Locate every blood parasite and identify its species.
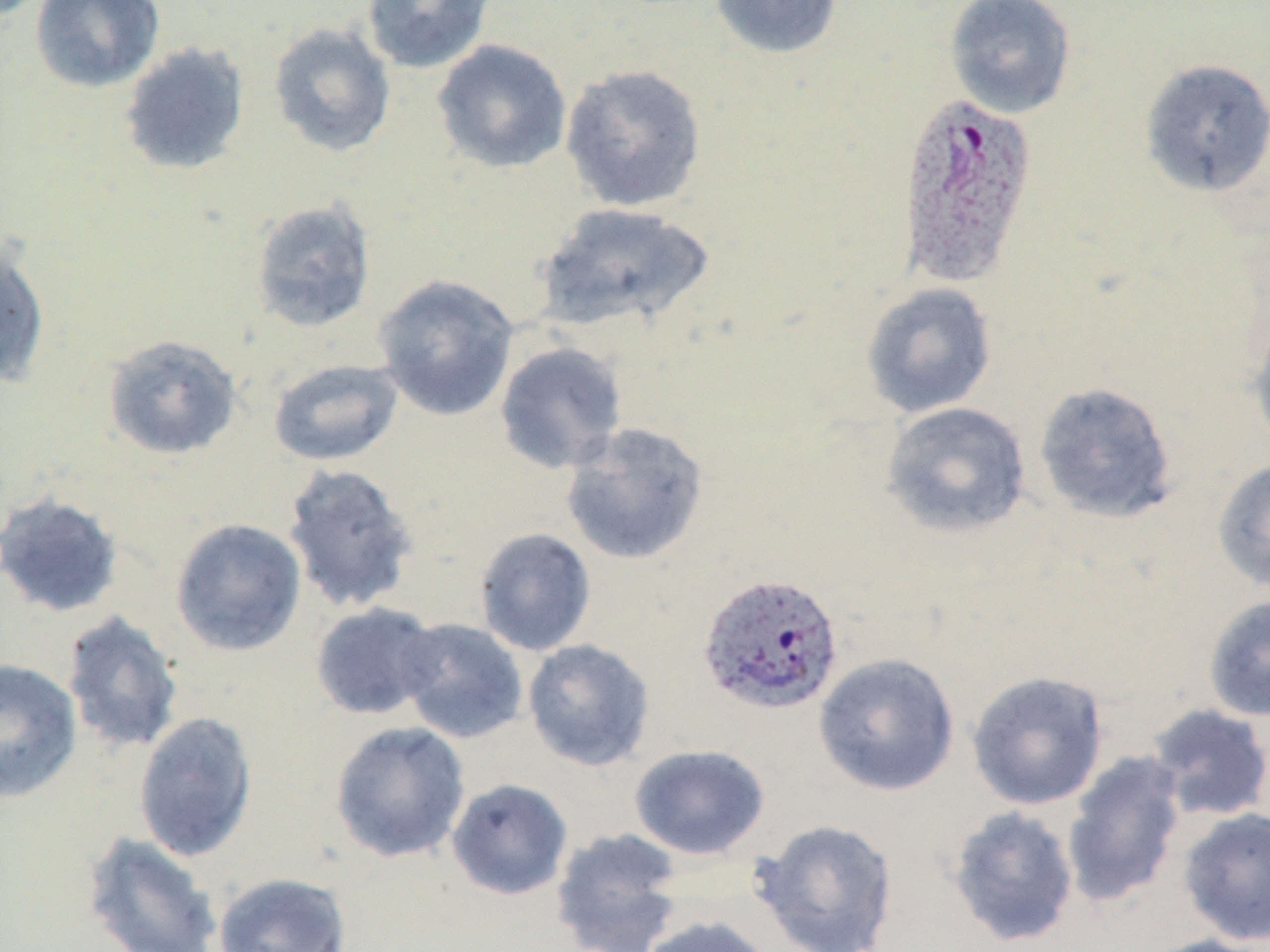

Approximate bounding boxes as (x1, y1, x2, y2) in pixels.
Plasmodium ovale-infected red blood cells: (895, 92, 1039, 289), (697, 572, 845, 715).
No Plasmodium falciparum, Plasmodium malariae, Plasmodium vivax, Babesia divergens, or Trypanosoma brucei observed.

Uninfected red blood cell locations: (30, 0, 165, 92), (361, 0, 495, 74), (707, 0, 844, 60), (944, 0, 1077, 119), (268, 22, 396, 158), (432, 39, 572, 173), (118, 41, 250, 176), (1139, 58, 1270, 197), (559, 63, 708, 213), (249, 198, 377, 333), (536, 202, 713, 334), (0, 239, 51, 390), (373, 273, 520, 420), (860, 282, 997, 418), (1248, 318, 1270, 453), (102, 334, 243, 460), (494, 341, 628, 475), (268, 358, 404, 466), (1033, 381, 1178, 524), (880, 401, 1032, 538), (560, 422, 709, 566), (1211, 458, 1270, 592), (281, 462, 420, 614), (0, 492, 124, 619), (170, 518, 307, 657), (474, 527, 597, 656), (1202, 594, 1270, 722), (309, 602, 443, 720), (61, 610, 184, 756), (395, 617, 529, 744), (522, 639, 655, 771), (813, 652, 960, 796), (0, 659, 83, 803), (965, 670, 1109, 810), (1146, 703, 1270, 823), (134, 710, 259, 864), (329, 721, 471, 862), (629, 744, 770, 860), (1061, 752, 1187, 909), (446, 778, 574, 900), (945, 805, 1080, 948), (1178, 807, 1270, 946), (751, 818, 899, 952), (550, 827, 686, 952), (81, 832, 222, 952), (213, 871, 352, 952), (638, 914, 778, 952), (1136, 934, 1270, 952). Slide-level diagnosis: Plasmodium ovale. Image is 1270×952 pixels. Optical microscopy. Thin blood film. One field of a larger specimen. Captured at 1000x magnification. May-Grünwald-Giemsa-stained preparation.